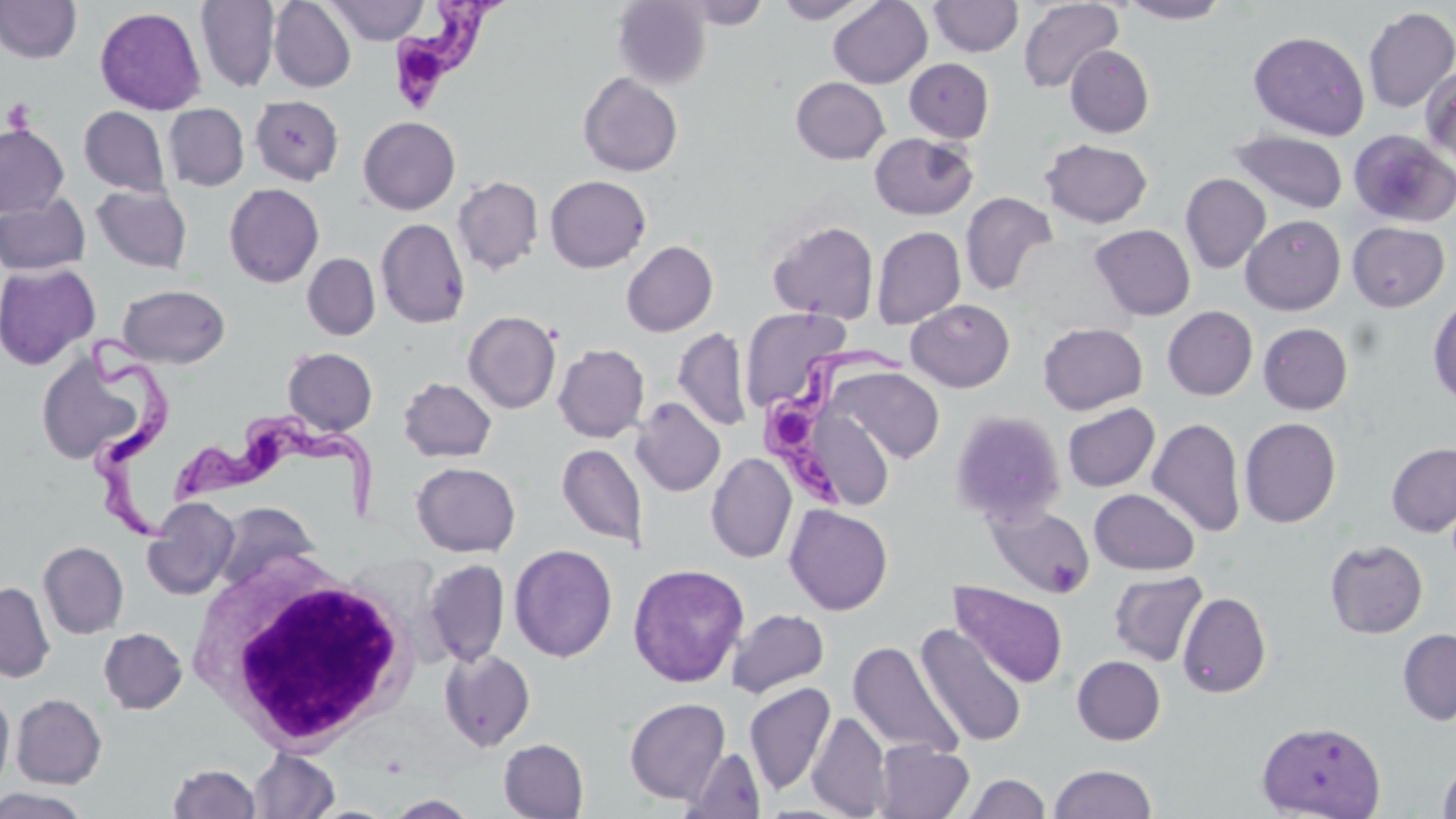 Approximate bounding boxes as (x1,y1)-(x2,y2) corner pairs in pixels. White blood cell locations: (186,550)-(423,754). Trypanosoma brucei locations: (391,0)-(507,116), (83,325)-(177,552), (765,340)-(922,513), (173,415)-(385,530). Platelet locations: (2,98)-(37,133). Uninfected red blood cell locations: (195,0)-(280,92), (269,0)-(356,92), (324,0)-(429,45), (776,0)-(869,23), (828,0)-(932,88), (928,0)-(1023,57), (1017,0)-(1124,93), (1119,0)-(1230,24), (0,1)-(82,64), (612,1)-(712,89), (678,1)-(771,29), (1362,6)-(1456,113), (95,7)-(206,115), (1248,30)-(1369,140), (1065,45)-(1154,138), (904,58)-(994,143), (1420,65)-(1456,170), (578,72)-(683,176), (791,77)-(890,164), (250,94)-(343,185), (164,103)-(249,191), (79,106)-(170,197), (358,116)-(460,215), (0,124)-(69,216), (1348,128)-(1456,228), (1230,130)-(1348,215), (869,133)-(978,220), (1039,138)-(1153,229), (1180,173)-(1270,274), (544,175)-(651,273), (452,176)-(544,275), (224,183)-(324,288), (91,185)-(192,273), (960,191)-(1058,296), (0,194)-(91,275), (1241,215)-(1346,314), (376,218)-(470,328), (767,220)-(879,322), (1347,222)-(1450,312), (1090,224)-(1196,321), (871,226)-(966,329), (621,240)-(718,336), (302,253)-(380,340), (0,262)-(100,370), (117,284)-(230,368), (1428,296)-(1456,405), (906,299)-(1015,392), (1162,306)-(1258,400), (740,307)-(850,411), (463,310)-(561,414), (1038,322)-(1148,414), (1258,323)-(1353,414), (672,327)-(752,432), (553,343)-(649,442), (283,347)-(378,436), (36,349)-(149,466), (827,365)-(945,464), (398,377)-(497,462), (631,397)-(726,497), (794,398)-(896,512), (1063,403)-(1160,492), (950,410)-(1067,527), (1147,418)-(1246,537), (1239,418)-(1341,528), (1386,442)-(1456,536), (557,444)-(647,547), (706,453)-(797,563), (411,462)-(520,557), (1089,488)-(1199,575), (142,497)-(240,600), (211,500)-(320,594), (987,503)-(1095,598), (785,504)-(893,615), (1325,539)-(1428,638), (38,541)-(129,639), (508,543)-(618,662), (509,549)-(750,671), (422,559)-(510,667), (628,563)-(749,688), (1108,571)-(1207,666), (0,581)-(55,682), (950,581)-(1068,688), (1177,591)-(1271,698), (726,608)-(829,698), (915,623)-(1027,747), (99,627)-(187,714), (1397,628)-(1456,725), (848,641)-(963,760), (439,649)-(536,751), (1072,655)-(1166,745), (744,682)-(836,796), (0,689)-(14,793), (11,693)-(106,788), (624,697)-(731,804), (807,711)-(891,818), (1256,720)-(1386,819), (498,738)-(589,818), (873,740)-(974,819), (681,747)-(767,818), (249,748)-(341,818), (1437,758)-(1456,819), (168,763)-(261,819), (1049,763)-(1157,819), (961,773)-(1051,818), (0,788)-(91,818), (385,794)-(479,818). Slide-level diagnosis: Trypanosoma brucei. Image is 1456×819 pixels. May-Grünwald-Giemsa-stained preparation. One field of a larger specimen. Captured at 1000x magnification. Light microscopy. Thin blood smear.